Give the preparation type.
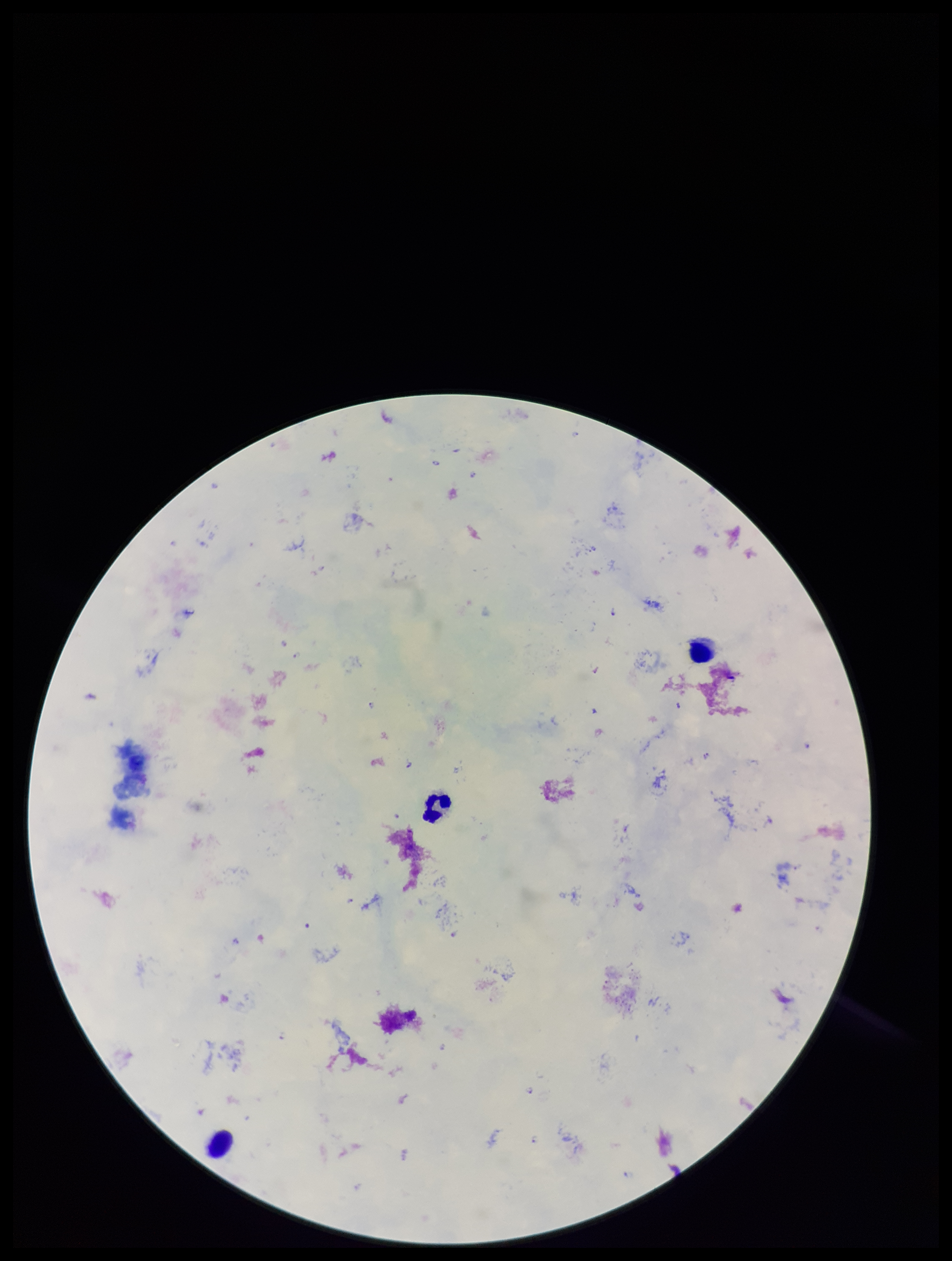
A thick smear.

Plasmodium parasites: seen. One field from this slide. Photographed through the microscope eyepiece with a smartphone camera. Species reported for this patient: Plasmodium falciparum. Giemsa stain. Patient malaria status: infected. Parasite count: 10. Leukocyte count: 3. Image is 952×1261 pixels.